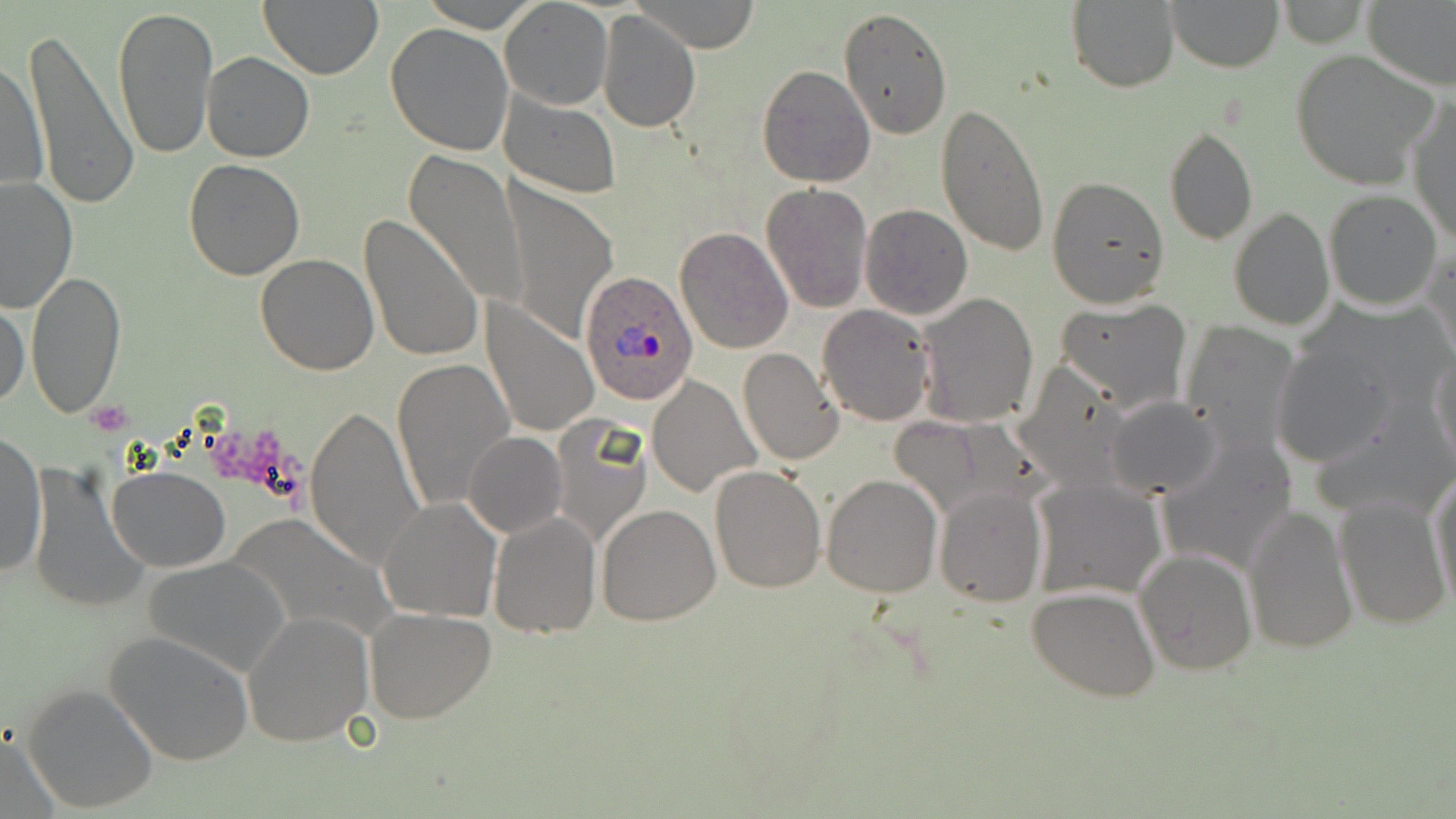

Summary:
  - Coordinate format: approximate bounding boxes as named x1/y1/x2/y2 corners in pixels
  - Uninfected red blood cell locations: (x1=257, y1=0, x2=385, y2=79), (x1=422, y1=0, x2=542, y2=32), (x1=499, y1=0, x2=612, y2=110), (x1=1065, y1=0, x2=1181, y2=94), (x1=1363, y1=0, x2=1456, y2=91), (x1=635, y1=1, x2=760, y2=53), (x1=1168, y1=1, x2=1282, y2=72), (x1=1276, y1=1, x2=1370, y2=49), (x1=113, y1=5, x2=216, y2=160), (x1=839, y1=7, x2=954, y2=140), (x1=596, y1=8, x2=701, y2=134), (x1=384, y1=22, x2=514, y2=158), (x1=22, y1=25, x2=138, y2=210), (x1=1290, y1=50, x2=1438, y2=188), (x1=203, y1=51, x2=314, y2=162), (x1=3, y1=57, x2=48, y2=200), (x1=756, y1=64, x2=875, y2=187), (x1=498, y1=89, x2=620, y2=198), (x1=1408, y1=93, x2=1455, y2=244), (x1=936, y1=104, x2=1050, y2=259), (x1=1164, y1=124, x2=1257, y2=247), (x1=403, y1=151, x2=529, y2=307), (x1=184, y1=158, x2=306, y2=280), (x1=1047, y1=176, x2=1170, y2=308), (x1=1, y1=177, x2=77, y2=314), (x1=501, y1=180, x2=617, y2=346), (x1=761, y1=182, x2=874, y2=313), (x1=1324, y1=188, x2=1444, y2=310), (x1=859, y1=202, x2=975, y2=319), (x1=1227, y1=207, x2=1334, y2=331), (x1=358, y1=214, x2=485, y2=364), (x1=676, y1=226, x2=794, y2=355), (x1=1423, y1=243, x2=1456, y2=368), (x1=255, y1=253, x2=380, y2=375), (x1=25, y1=270, x2=126, y2=419), (x1=915, y1=292, x2=1039, y2=430), (x1=1055, y1=297, x2=1194, y2=416), (x1=481, y1=299, x2=599, y2=441), (x1=1, y1=302, x2=29, y2=408), (x1=817, y1=304, x2=935, y2=427), (x1=1180, y1=320, x2=1303, y2=455), (x1=1270, y1=340, x2=1400, y2=469), (x1=738, y1=347, x2=845, y2=466), (x1=1430, y1=348, x2=1456, y2=479), (x1=391, y1=359, x2=513, y2=513), (x1=1014, y1=359, x2=1137, y2=489), (x1=646, y1=374, x2=759, y2=497), (x1=1105, y1=396, x2=1224, y2=501), (x1=304, y1=405, x2=426, y2=570), (x1=1119, y1=407, x2=1269, y2=542), (x1=550, y1=413, x2=651, y2=544), (x1=0, y1=432, x2=48, y2=580), (x1=463, y1=432, x2=567, y2=539), (x1=1155, y1=434, x2=1298, y2=576), (x1=24, y1=463, x2=150, y2=613), (x1=709, y1=463, x2=826, y2=593), (x1=1429, y1=467, x2=1456, y2=611), (x1=106, y1=468, x2=230, y2=572), (x1=822, y1=473, x2=942, y2=596), (x1=1031, y1=478, x2=1167, y2=602), (x1=934, y1=486, x2=1046, y2=606), (x1=1333, y1=494, x2=1450, y2=631), (x1=377, y1=498, x2=503, y2=623), (x1=596, y1=503, x2=721, y2=626), (x1=1242, y1=505, x2=1359, y2=654), (x1=225, y1=511, x2=391, y2=644), (x1=487, y1=511, x2=601, y2=640), (x1=1133, y1=549, x2=1258, y2=678), (x1=145, y1=555, x2=292, y2=678), (x1=1026, y1=586, x2=1159, y2=700), (x1=364, y1=607, x2=497, y2=724), (x1=243, y1=609, x2=374, y2=746), (x1=103, y1=630, x2=255, y2=767), (x1=21, y1=682, x2=159, y2=813), (x1=1, y1=726, x2=64, y2=819)
  - Platelet locations: (x1=86, y1=401, x2=134, y2=435), (x1=209, y1=432, x2=305, y2=491)
  - Plasmodium ovale-infected red blood cell locations: (x1=580, y1=273, x2=699, y2=405)
  - Slide-level diagnosis: Plasmodium ovale
  - Modality: light microscopy
  - Field of view: one of a larger specimen
  - Preparation: thin blood film
  - Magnification: 1000x
  - Image size: 1456×819 pixels
  - Stain: May-Grünwald-Giemsa